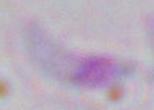

Summary:
  - Modality: photomicrograph
  - Magnification: 1000x
  - Identification: Toxoplasma gondii